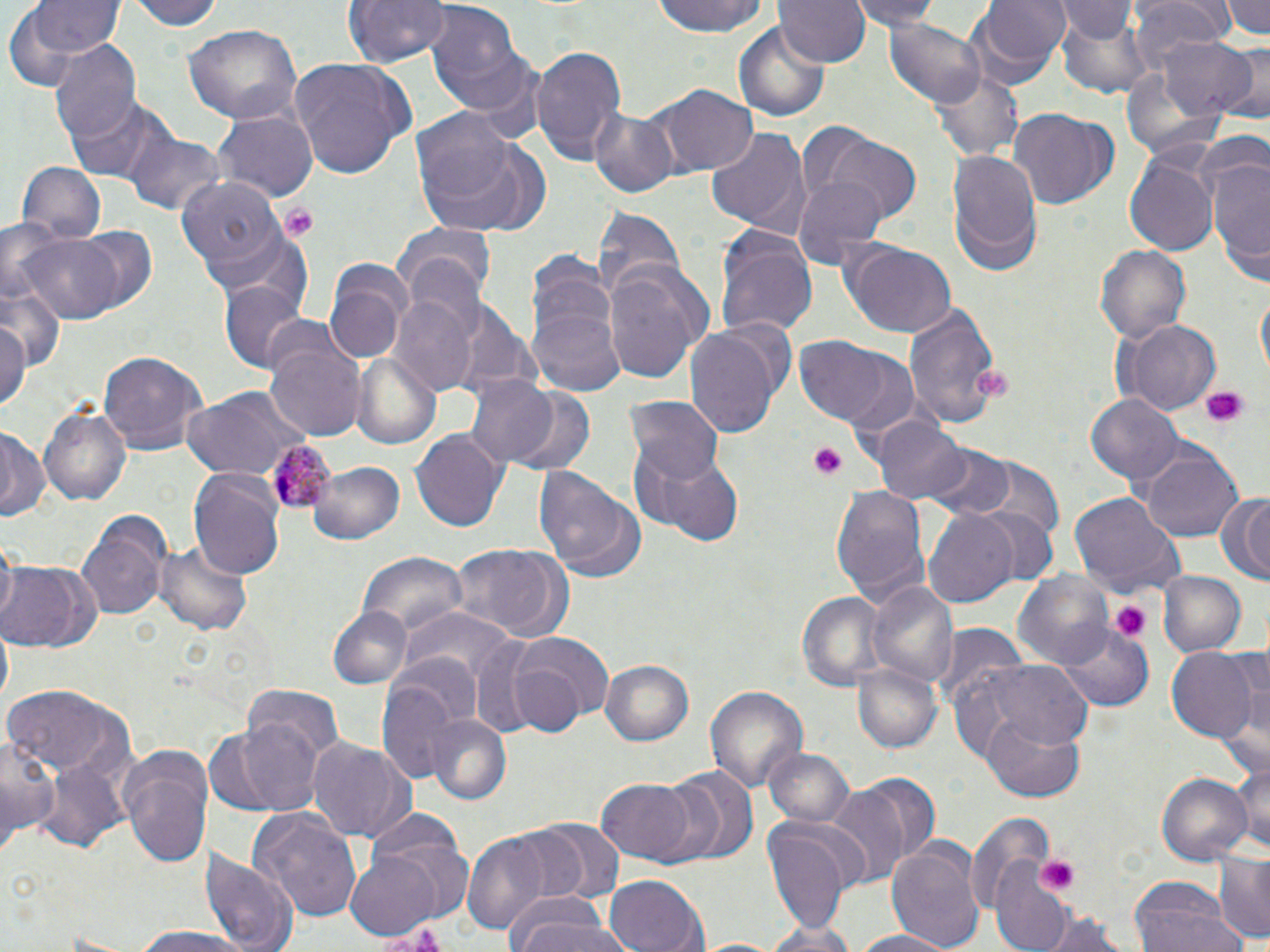
Approximate bounding boxes as (x1, y1, x2, y2) in pixels. Uninfected red blood cell locations: (133, 0, 226, 31), (345, 0, 448, 68), (649, 0, 773, 39), (776, 0, 872, 68), (850, 0, 945, 33), (974, 0, 1069, 77), (1131, 0, 1229, 72), (1221, 0, 1270, 41), (20, 1, 122, 67), (426, 1, 539, 123), (1059, 2, 1139, 46), (1056, 8, 1148, 98), (887, 20, 990, 110), (186, 25, 299, 122), (736, 26, 830, 121), (1162, 36, 1261, 121), (48, 42, 143, 143), (1219, 43, 1270, 126), (531, 44, 627, 168), (288, 56, 417, 180), (1122, 60, 1227, 164), (931, 64, 1023, 161), (654, 85, 758, 176), (65, 93, 172, 184), (587, 102, 680, 197), (1009, 109, 1119, 210), (215, 110, 315, 202), (410, 111, 545, 238), (801, 125, 924, 228), (705, 126, 808, 233), (123, 129, 221, 215), (1192, 132, 1269, 206), (947, 146, 1040, 271), (1205, 148, 1270, 276), (1122, 153, 1218, 256), (17, 162, 106, 244), (175, 176, 282, 275), (792, 177, 886, 267), (594, 206, 687, 303), (202, 224, 310, 309), (72, 225, 159, 314), (397, 225, 497, 302), (715, 226, 817, 339), (17, 230, 127, 323), (840, 240, 956, 337), (1096, 244, 1194, 343), (524, 250, 622, 375), (326, 260, 411, 361), (602, 265, 707, 385), (220, 280, 309, 374), (0, 284, 67, 374), (1256, 289, 1269, 380), (392, 296, 480, 396), (901, 299, 1003, 432), (529, 305, 628, 397), (0, 313, 29, 411), (685, 320, 787, 435), (1113, 320, 1220, 414), (791, 334, 906, 429), (265, 339, 366, 440), (98, 350, 209, 456), (838, 353, 923, 442), (350, 356, 439, 447), (460, 372, 569, 470), (498, 385, 597, 476), (181, 387, 311, 479), (1087, 394, 1184, 484), (627, 396, 722, 484), (38, 401, 132, 510), (869, 416, 968, 506), (0, 426, 46, 523), (411, 428, 508, 534), (630, 442, 741, 544), (924, 443, 1016, 520), (1141, 448, 1243, 544), (964, 456, 1068, 543), (309, 460, 404, 546), (532, 467, 645, 584), (188, 469, 285, 578), (831, 485, 930, 610), (1070, 492, 1186, 599), (1216, 493, 1270, 585), (970, 504, 1059, 590), (924, 509, 1020, 608), (75, 514, 170, 623), (154, 540, 252, 635), (446, 543, 574, 644), (358, 554, 469, 643), (1, 561, 102, 653), (1156, 570, 1247, 658), (1012, 573, 1110, 666), (867, 581, 959, 689), (793, 591, 884, 691), (326, 605, 413, 690), (402, 606, 514, 683), (934, 623, 1029, 718), (1057, 624, 1152, 710), (0, 627, 13, 705), (509, 632, 615, 729), (467, 636, 559, 740), (1167, 648, 1258, 742), (1223, 648, 1270, 769), (599, 658, 696, 747), (956, 661, 1092, 755), (852, 662, 942, 756), (375, 679, 467, 779), (236, 681, 342, 790), (2, 682, 131, 777), (704, 685, 807, 798), (424, 714, 513, 805), (981, 715, 1085, 802), (210, 719, 322, 816), (0, 728, 61, 847), (307, 737, 416, 843), (116, 741, 212, 869), (763, 746, 856, 827), (36, 750, 133, 854), (1228, 751, 1270, 853), (665, 769, 755, 863), (843, 770, 942, 872), (1155, 770, 1253, 867), (597, 779, 697, 862), (824, 787, 911, 887), (252, 809, 362, 922), (965, 811, 1055, 915), (360, 814, 475, 918), (762, 815, 860, 931), (528, 820, 622, 899), (463, 829, 560, 938), (886, 840, 986, 952), (201, 845, 298, 952), (344, 852, 443, 939), (1215, 854, 1270, 944), (991, 858, 1078, 949), (605, 874, 707, 952), (1130, 876, 1239, 952), (507, 894, 622, 952), (1036, 908, 1133, 952), (763, 919, 859, 952), (129, 923, 258, 951), (849, 928, 959, 952). Platelet locations: (280, 202, 317, 242), (972, 367, 1016, 398), (1199, 386, 1250, 429), (809, 442, 849, 480), (1109, 600, 1149, 642), (1035, 855, 1080, 896). Plasmodium malariae-infected red blood cell locations: (268, 441, 335, 513). Slide-level diagnosis: Plasmodium malariae. Thin blood film. 1000x magnification. Light microscopy. May-Grünwald-Giemsa stain. Image is 1270×952 pixels. Single field of view.